Evaluate for parasitized red blood cells.
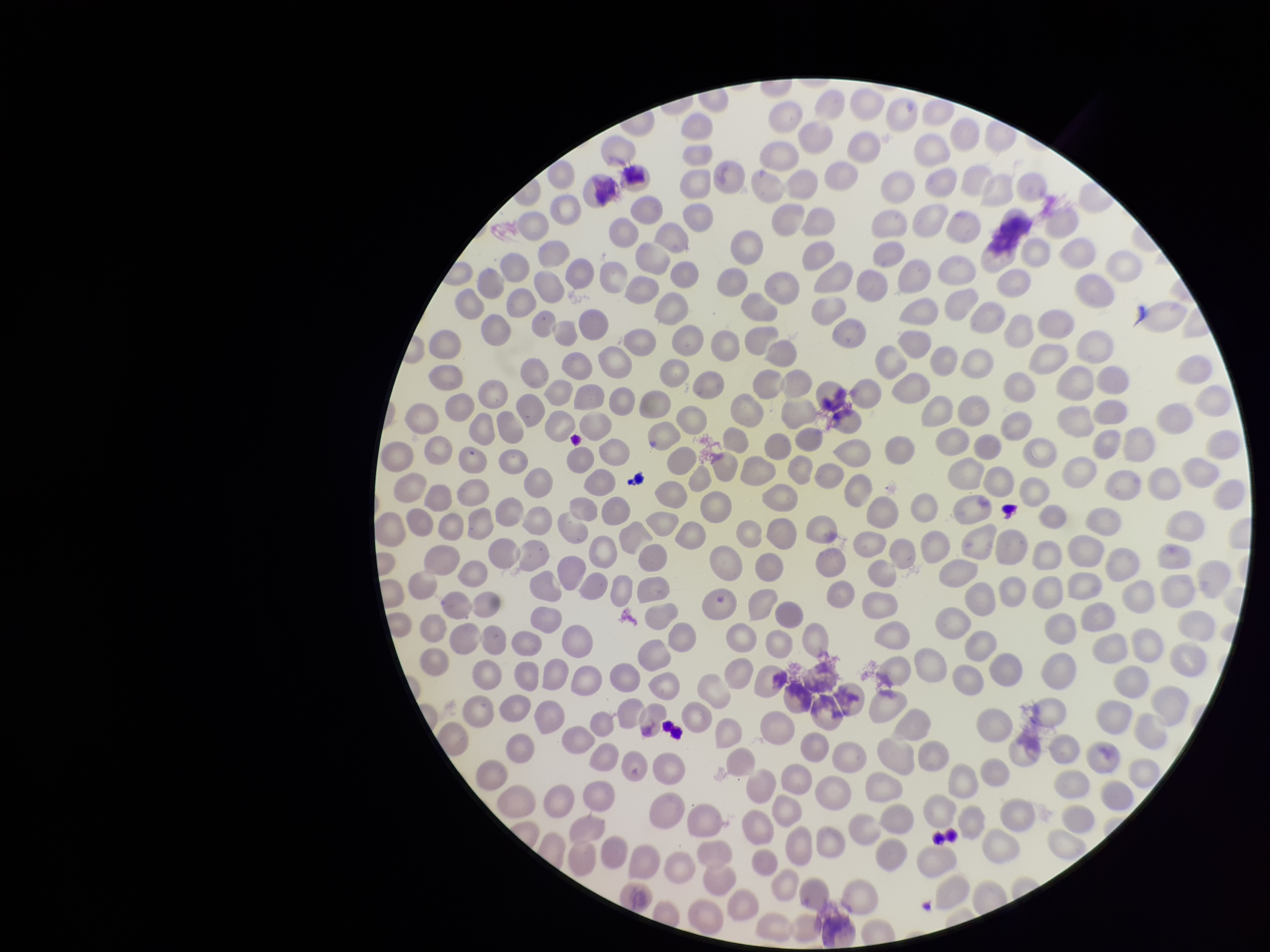
None identified.

Image is 1270×952 pixels. Species reported for this patient: Plasmodium vivax. Preparation: thin smear. Giemsa stain. Smartphone photograph taken through the eyepiece of a microscope. Red blood cell count: 268. Patient malaria status: positive. Single field of view. Parasitized red blood cell count: 0.